Give the position of every leukocyte visible.
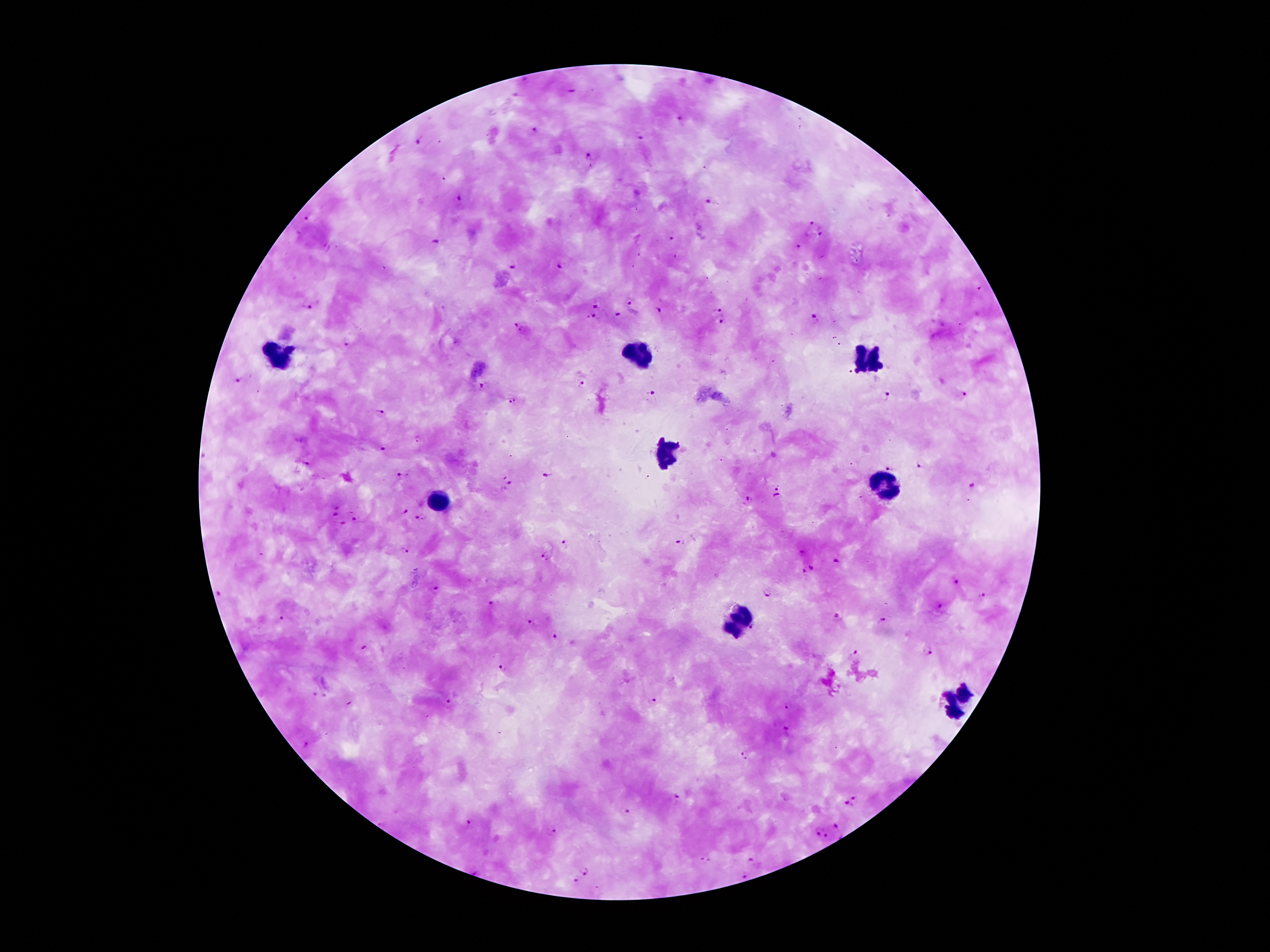
Approximate centers as {x, y} in pixels.
Leukocytes: {640, 355}, {278, 359}, {866, 359}, {666, 451}, {884, 487}, {440, 503}, {740, 621}, {959, 703}.

Summary:
  - Malaria parasite locations: {570, 92}, {520, 94}, {680, 119}, {534, 130}, {639, 137}, {419, 141}, {588, 156}, {462, 199}, {708, 200}, {307, 218}, {813, 223}, {820, 232}, {673, 240}, {433, 243}, {797, 245}, {513, 263}, {560, 267}, {630, 300}, {596, 301}, {308, 303}, {721, 310}, {658, 312}, {619, 315}, {592, 317}, {814, 318}, {719, 324}, {518, 327}, {345, 342}, {849, 373}, {239, 380}, {581, 383}, {481, 385}, {652, 394}, {963, 395}, {884, 399}, {513, 401}, {380, 413}, {382, 449}, {304, 464}, {920, 464}, {889, 466}, {546, 473}, {401, 475}, {511, 482}, {777, 487}, {972, 487}, {777, 496}, {751, 499}, {405, 510}, {335, 512}, {420, 517}, {355, 518}, {342, 523}, {676, 541}, {563, 543}, {404, 550}, {803, 550}, {544, 557}, {837, 560}, {813, 567}, {803, 571}, {956, 581}, {435, 590}, {768, 592}, {218, 595}, {983, 597}, {493, 605}, {941, 609}, {838, 618}, {282, 619}, {883, 622}, {529, 623}, {753, 628}, {555, 636}, {926, 652}, {853, 653}, {504, 667}, {653, 700}, {451, 703}, {788, 705}, {789, 732}, {308, 744}, {748, 754}, {676, 797}, {855, 797}, {846, 804}, {624, 811}, {467, 821}, {837, 824}, {552, 830}, {821, 834}, {704, 860}, {750, 861}, {585, 870}, {742, 876}, {575, 881}
  - Magnification: 100x
  - Image size: 1270×952 pixels
  - Field of view: single
  - Patient malaria status: positive for Plasmodium falciparum
  - Capture: smartphone through the microscope eyepiece
  - Preparation: thick blood smear
  - Stain: Giemsa